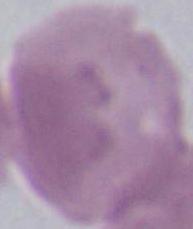
{
  "modality": "photomicrograph",
  "magnification": "1000x",
  "identification": "erythrocyte"
}